Give the position of every leukocyte visible.
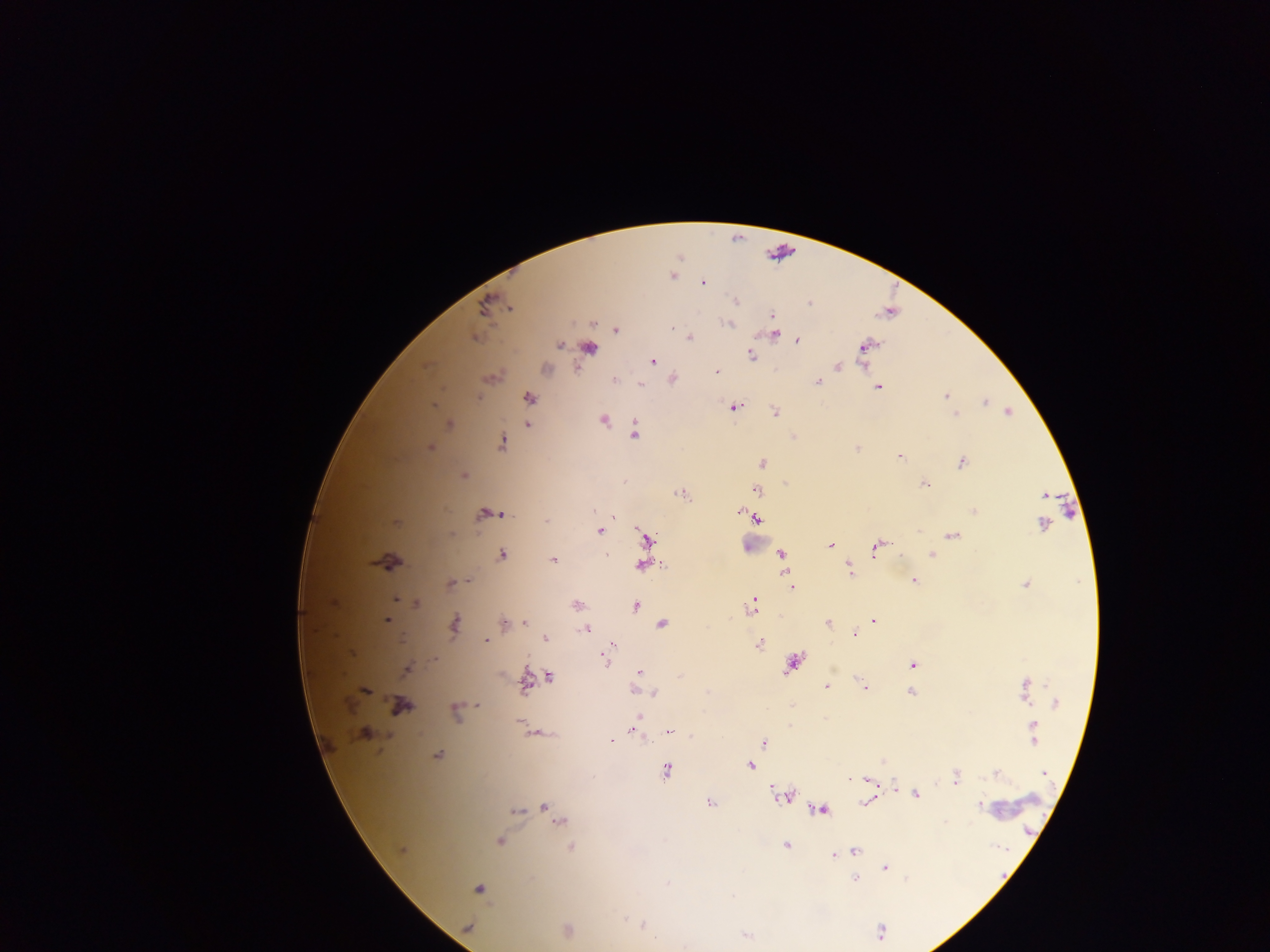

No leukocytes observed.

Approximate centers as x y in pixels. Plasmodium parasite locations: 672 276; 703 283; 736 301; 809 303; 772 316; 727 324; 672 328; 616 330; 774 334; 689 337; 797 341; 560 345; 865 346; 590 348; 750 355; 652 361; 837 366; 545 369; 716 372; 673 379; 615 380; 818 382; 641 384; 878 387; 946 396; 478 398; 529 398; 985 402; 433 405; 735 407; 1008 411; 774 412; 955 414; 603 420; 448 425; 528 425; 635 433; 502 443; 430 447; 857 447; 900 456; 762 463; 962 463; 463 476; 924 484; 758 490; 682 494; 1044 495; 974 510; 740 512; 490 514; 500 514; 747 515; 613 517; 757 518; 546 522; 396 523; 1043 525; 599 531; 953 535; 647 540; 830 546; 877 546; 781 555; 932 555; 502 556; 554 560; 390 562; 643 565; 850 569; 914 581; 450 583; 1026 585; 792 587; 395 600; 333 603; 417 603; 576 605; 636 605; 750 607; 387 620; 874 621; 525 622; 828 622; 504 623; 455 624; 663 624; 587 629; 855 634; 545 638; 486 641; 759 644; 613 645; 609 649; 604 657; 434 659; 793 663; 912 665; 407 670; 639 672; 680 675; 550 676; 526 682; 1027 685; 863 686; 827 687; 365 690; 635 690; 910 692; 654 693; 1025 696; 1056 703; 478 705; 401 706; 455 711; 638 717; 520 724; 1033 730; 637 731; 536 732; 670 732; 364 733; 612 740; 764 743; 438 755; 883 762; 750 765; 667 770; 996 772; 1044 773; 955 777; 850 778; 866 778; 894 787; 783 795; 916 795; 865 802; 711 803; 979 806; 545 807; 516 810; 821 810; 559 820; 500 842; 786 845; 570 847; 401 850; 856 850; 834 855; 856 861; 885 867; 855 880; 668 882; 479 889; 625 919; 642 925; 468 927; 568 931; 881 932; 746 936. Collected in Ghana. Thick blood smear. Mobile-phone photograph taken through the microscope. One field of view. Image is 1270×952 pixels.